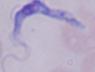
Captured at 1000x magnification. Photomicrograph. A trypanosome is seen.